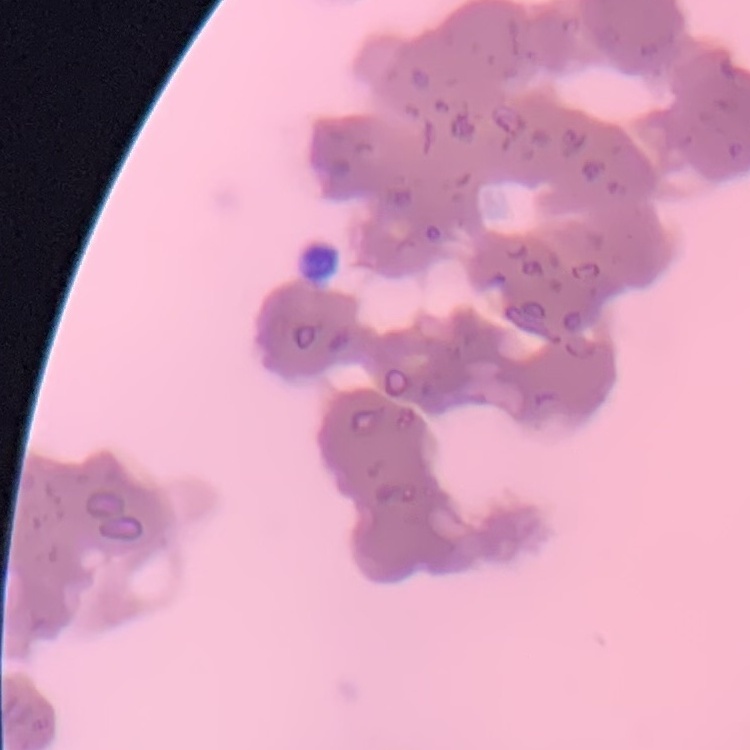 The erythrocytes exhibit rouleaux formation. Thin blood film. Field's or Giemsa stain. Square crop of a larger photomicrograph.